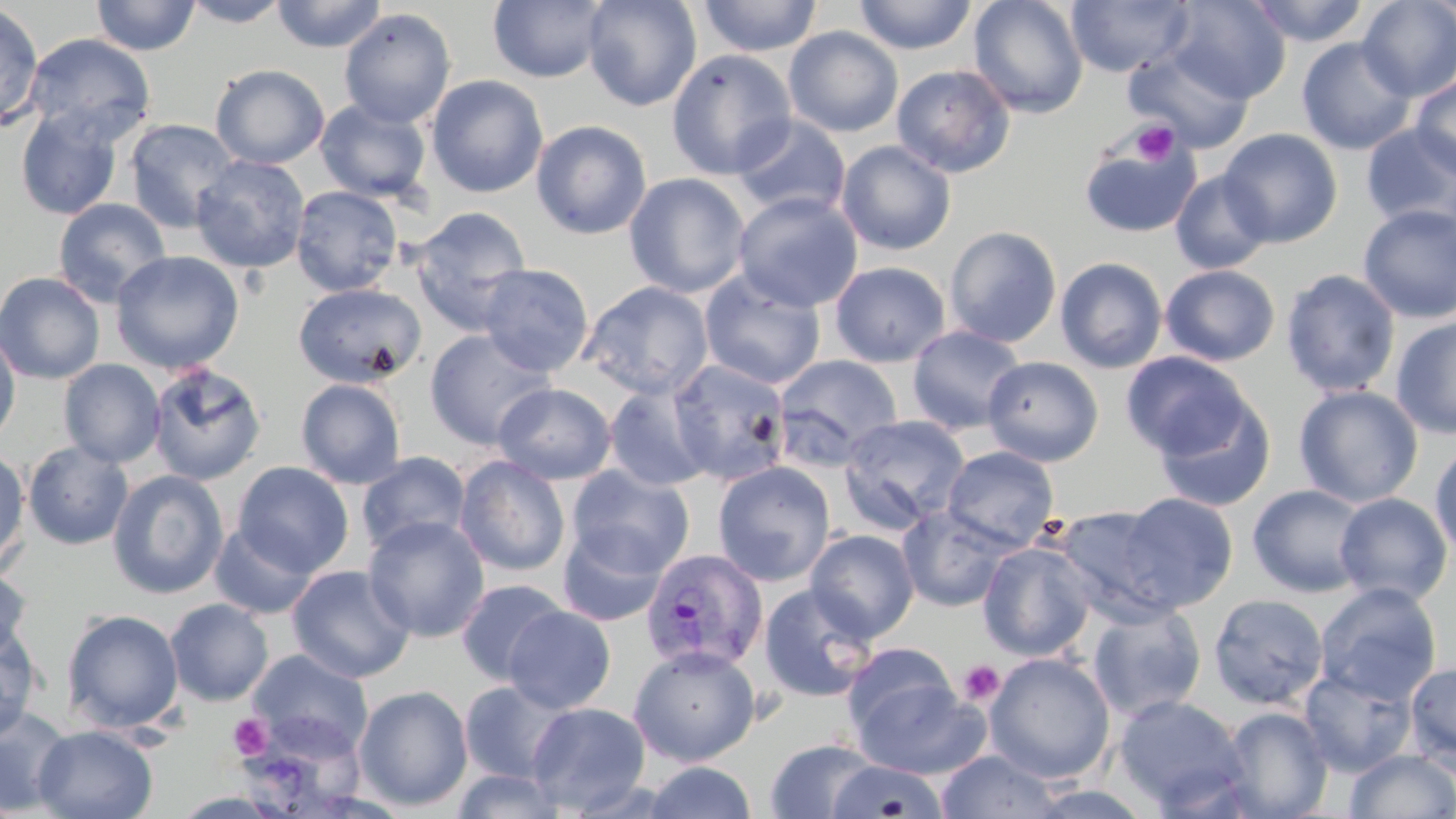

{
  "slide_level_diagnosis": "Plasmodium vivax",
  "preparation": "thin blood smear",
  "stain": "May-Grünwald-Giemsa",
  "uninfected_red_blood_cell_locations": "approximate bounding boxes as (x1,y1)-(x2,y2) corner pairs in pixels: (90,0)-(201,56), (180,0)-(292,27), (271,0)-(387,53), (488,0)-(610,83), (582,0)-(703,111), (696,0)-(823,57), (853,0)-(978,55), (969,0)-(1089,119), (1066,0)-(1195,78), (1168,0)-(1291,103), (1245,0)-(1370,46), (1356,0)-(1456,101), (0,2)-(45,131), (338,8)-(456,129), (784,26)-(904,137), (21,33)-(156,144), (1296,37)-(1417,155), (1124,45)-(1256,154), (666,49)-(797,180), (210,63)-(330,169), (891,64)-(1016,178), (426,75)-(548,198), (1410,77)-(1456,180), (315,99)-(432,203), (15,107)-(124,221), (732,114)-(851,219), (124,118)-(242,233), (531,119)-(652,240), (1361,122)-(1456,232), (1217,128)-(1343,248), (1079,133)-(1202,238), (836,140)-(957,256), (190,155)-(310,273), (1170,169)-(1274,274), (623,172)-(751,298), (291,186)-(404,297), (732,191)-(864,312), (52,198)-(172,307), (1358,205)-(1456,324), (410,206)-(533,331), (944,226)-(1062,347), (111,250)-(245,373), (1055,257)-(1168,373), (829,261)-(951,367), (476,263)-(594,376), (1160,264)-(1280,366), (1281,269)-(1400,397), (699,270)-(826,390), (0,271)-(106,385), (580,281)-(714,401), (292,282)-(427,389), (1391,316)-(1456,439), (906,325)-(1027,435), (0,326)-(21,448), (424,327)-(557,451), (1121,352)-(1254,460), (773,354)-(902,468), (982,356)-(1103,466), (58,359)-(166,468), (666,361)-(791,488), (147,362)-(267,485), (295,378)-(406,489), (493,383)-(616,484), (603,385)-(714,492), (1293,385)-(1424,508), (1153,394)-(1276,511), (838,414)-(971,534), (22,440)-(134,550), (1429,441)-(1456,562), (0,445)-(31,576), (942,446)-(1059,550), (356,451)-(471,557), (454,455)-(571,577), (232,461)-(354,577), (713,461)-(835,586), (566,464)-(695,581), (107,470)-(228,599), (1247,484)-(1371,598), (1113,492)-(1238,612), (1335,492)-(1453,606), (897,504)-(1016,612), (1052,504)-(1186,624), (363,515)-(490,642), (209,522)-(320,620), (557,524)-(669,627), (805,529)-(919,641), (977,541)-(1097,661), (0,564)-(33,664), (287,565)-(414,683), (455,579)-(570,686), (758,582)-(881,703), (1314,582)-(1442,705), (1207,593)-(1329,710), (165,599)-(274,706), (1087,601)-(1207,722), (502,605)-(616,714), (61,608)-(184,734), (0,624)-(42,741), (842,642)-(959,743), (628,645)-(761,766), (248,649)-(373,758), (984,651)-(1116,784), (1404,662)-(1456,770), (1298,667)-(1416,776), (851,676)-(989,779), (458,680)-(572,785), (354,684)-(473,812), (1112,694)-(1250,814), (526,702)-(651,814), (1219,706)-(1334,819), (0,707)-(75,816), (241,719)-(368,819), (33,725)-(157,819), (765,738)-(884,818), (936,750)-(1064,819), (1344,750)-(1456,818), (643,761)-(757,819), (827,761)-(950,818), (449,768)-(569,818), (1021,784)-(1157,819)",
  "magnification": "1000x",
  "plasmodium_vivax_infected_red_blood_cell_locations": "approximate bounding boxes as (x1,y1)-(x2,y2) corner pairs in pixels: (640,548)-(769,673)",
  "modality": "optical microscopy",
  "image_size": "1456×819 pixels",
  "platelet_locations": "approximate bounding boxes as (x1,y1)-(x2,y2) corner pairs in pixels: (1130,121)-(1179,167), (958,659)-(1005,706), (229,713)-(273,760)",
  "field_of_view": "single"
}